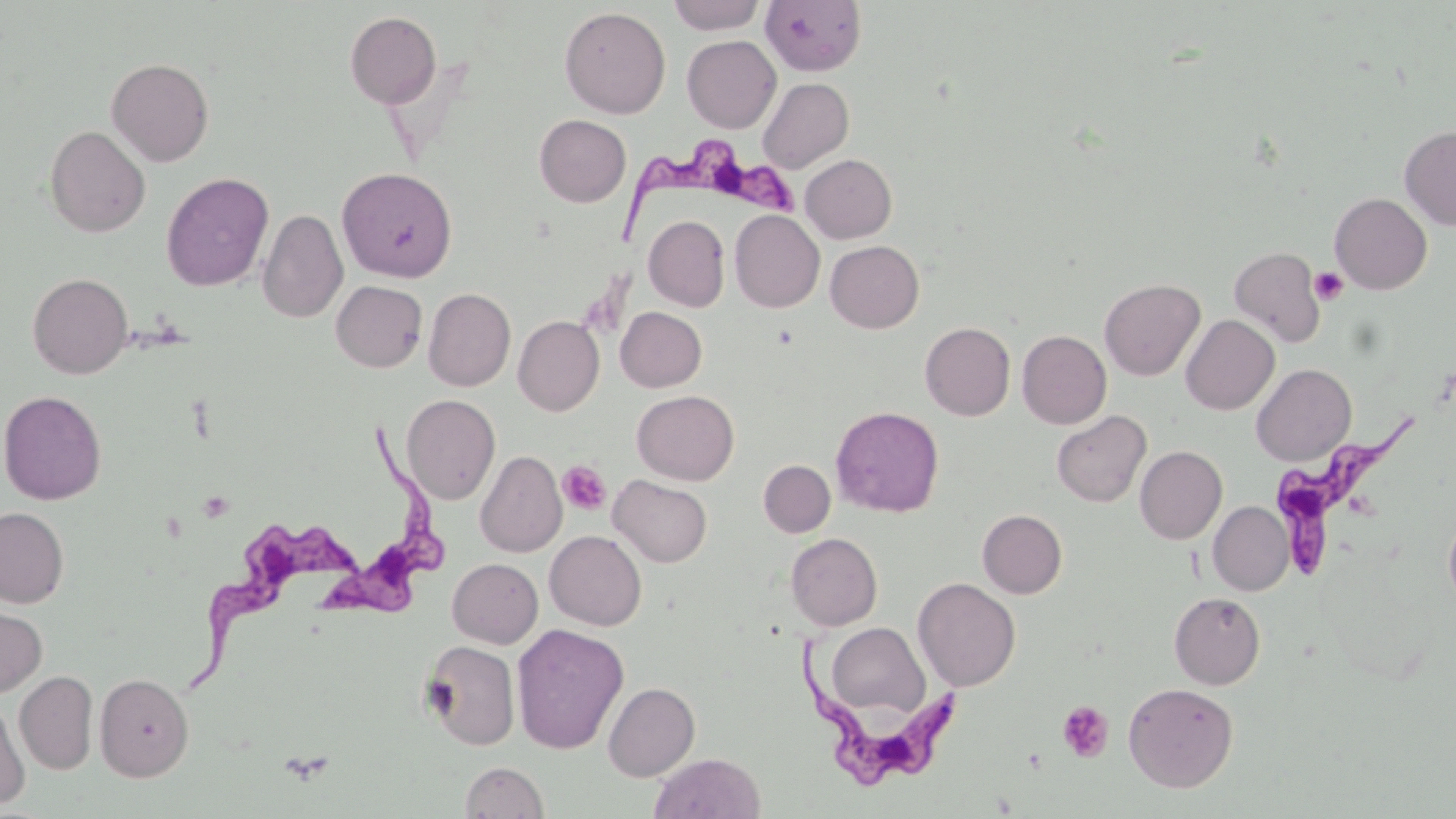

Summary:
  - Coordinate format: approximate bounding boxes as named x1/y1/x2/y2 corners in pixels
  - Trypanosoma brucei locations: (x1=619, y1=137, x2=803, y2=242), (x1=1271, y1=413, x2=1416, y2=584), (x1=320, y1=417, x2=450, y2=625), (x1=192, y1=513, x2=361, y2=696), (x1=800, y1=636, x2=967, y2=792)
  - Platelet locations: (x1=1309, y1=266, x2=1348, y2=305), (x1=558, y1=460, x2=612, y2=515), (x1=1056, y1=700, x2=1114, y2=762)
  - Uninfected red blood cell locations: (x1=667, y1=0, x2=765, y2=34), (x1=760, y1=1, x2=866, y2=75), (x1=559, y1=6, x2=670, y2=118), (x1=345, y1=11, x2=441, y2=108), (x1=682, y1=35, x2=781, y2=133), (x1=106, y1=57, x2=214, y2=166), (x1=757, y1=77, x2=854, y2=172), (x1=535, y1=114, x2=631, y2=207), (x1=1399, y1=124, x2=1456, y2=231), (x1=44, y1=125, x2=150, y2=237), (x1=801, y1=154, x2=897, y2=243), (x1=337, y1=167, x2=457, y2=282), (x1=161, y1=172, x2=273, y2=291), (x1=1330, y1=192, x2=1432, y2=294), (x1=257, y1=208, x2=348, y2=323), (x1=729, y1=210, x2=824, y2=312), (x1=644, y1=215, x2=730, y2=312), (x1=825, y1=240, x2=923, y2=333), (x1=1229, y1=246, x2=1327, y2=347), (x1=27, y1=273, x2=133, y2=379), (x1=1099, y1=278, x2=1205, y2=380), (x1=331, y1=280, x2=428, y2=372), (x1=423, y1=288, x2=515, y2=391), (x1=616, y1=307, x2=707, y2=392), (x1=1181, y1=315, x2=1279, y2=414), (x1=513, y1=316, x2=604, y2=415), (x1=920, y1=322, x2=1016, y2=420), (x1=1017, y1=330, x2=1112, y2=429), (x1=1251, y1=363, x2=1356, y2=465), (x1=0, y1=390, x2=106, y2=504), (x1=632, y1=390, x2=739, y2=485), (x1=401, y1=394, x2=500, y2=504), (x1=830, y1=406, x2=944, y2=517), (x1=1052, y1=410, x2=1151, y2=507), (x1=1135, y1=445, x2=1227, y2=544), (x1=476, y1=451, x2=567, y2=557), (x1=759, y1=460, x2=835, y2=537), (x1=609, y1=474, x2=712, y2=568), (x1=1208, y1=502, x2=1293, y2=595), (x1=0, y1=507, x2=69, y2=607), (x1=977, y1=509, x2=1067, y2=598), (x1=1443, y1=509, x2=1456, y2=613), (x1=545, y1=530, x2=646, y2=630), (x1=786, y1=533, x2=882, y2=630), (x1=448, y1=558, x2=543, y2=647), (x1=913, y1=577, x2=1021, y2=691), (x1=1169, y1=592, x2=1265, y2=689), (x1=0, y1=602, x2=47, y2=696), (x1=824, y1=622, x2=928, y2=719), (x1=511, y1=623, x2=629, y2=754), (x1=420, y1=639, x2=521, y2=751), (x1=14, y1=671, x2=98, y2=774), (x1=94, y1=672, x2=194, y2=781), (x1=603, y1=682, x2=700, y2=781), (x1=1123, y1=682, x2=1238, y2=792), (x1=0, y1=695, x2=30, y2=810), (x1=649, y1=751, x2=765, y2=818), (x1=460, y1=761, x2=548, y2=818)
  - Slide-level diagnosis: Trypanosoma brucei
  - Stain: May-Grünwald-Giemsa
  - Magnification: 1000x
  - Image size: 1456×819 pixels
  - Preparation: thin blood film
  - Modality: light microscopy
  - Field of view: one of a larger specimen